Outline each blood parasite and name the species.
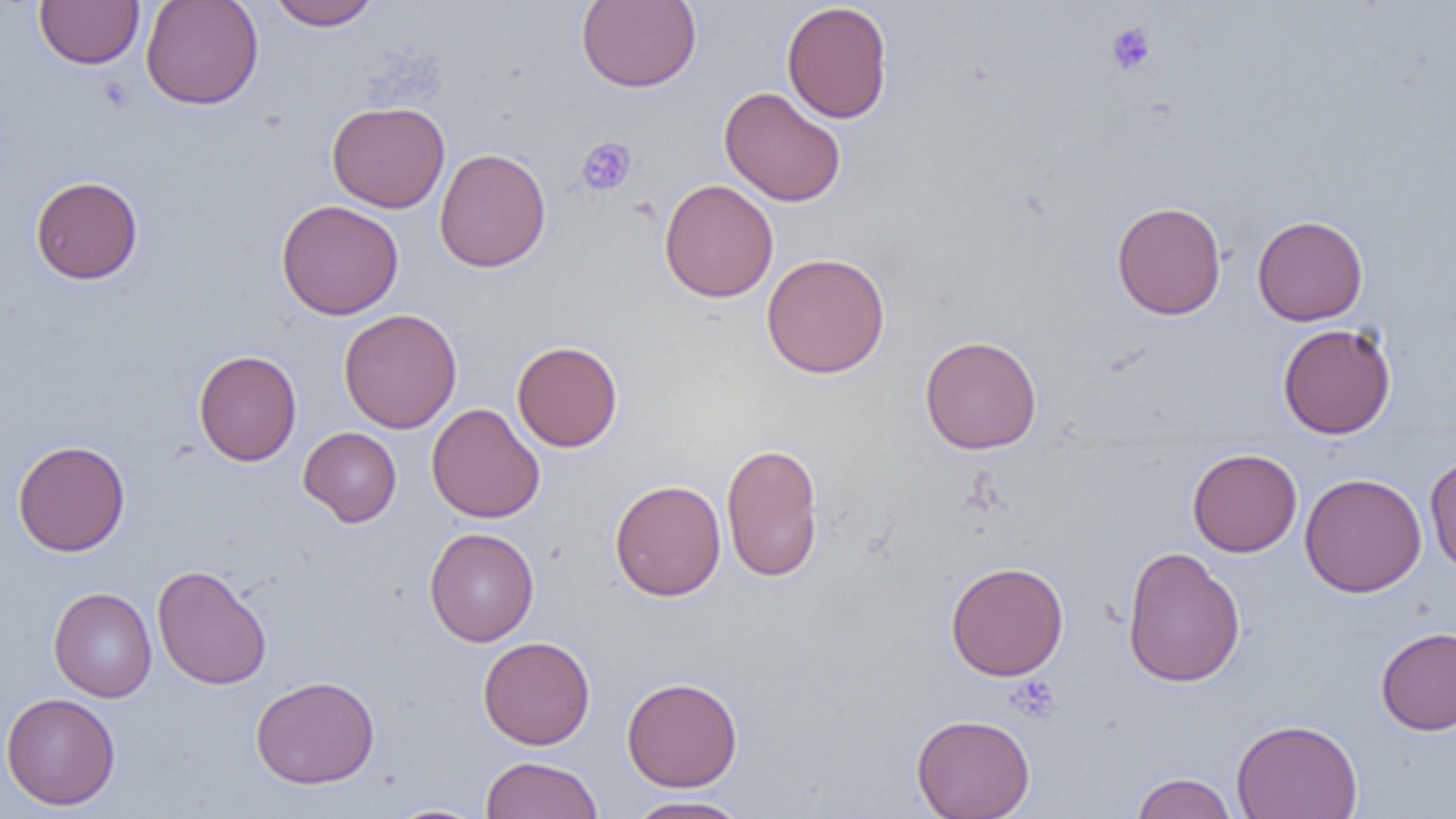
No blood parasites observed.

Summary:
  - Coordinate format: approximate bounding boxes as [x1, y1, x2, y2] in pixels
  - Uninfected red blood cell locations: [34, 0, 144, 69], [140, 0, 264, 110], [267, 0, 381, 30], [576, 0, 701, 92], [781, 1, 894, 124], [719, 86, 846, 207], [326, 101, 450, 213], [434, 147, 551, 272], [30, 176, 143, 285], [659, 179, 778, 302], [276, 200, 403, 320], [1111, 201, 1226, 320], [1252, 215, 1368, 326], [761, 253, 891, 379], [338, 309, 462, 433], [1277, 323, 1396, 439], [919, 335, 1041, 454], [511, 340, 623, 452], [193, 350, 302, 466], [426, 403, 545, 524], [298, 426, 402, 527], [12, 440, 130, 556], [721, 442, 824, 582], [1187, 448, 1302, 557], [1424, 452, 1456, 575], [1299, 472, 1427, 598], [609, 479, 726, 601], [424, 527, 539, 646], [1122, 545, 1245, 688], [945, 561, 1069, 680], [152, 564, 271, 690], [48, 588, 157, 702], [1375, 627, 1456, 735], [478, 636, 595, 750], [250, 675, 380, 789], [621, 676, 743, 792], [1, 692, 121, 810], [911, 713, 1035, 818], [1231, 718, 1363, 819], [481, 756, 603, 819], [1130, 772, 1238, 818], [624, 795, 752, 818], [380, 803, 493, 819]
  - Platelet locations: [1105, 21, 1157, 76], [576, 136, 638, 196], [1006, 676, 1061, 724]
  - Slide-level diagnosis: no evidence of blood parasites
  - Preparation: thin blood film
  - Image size: 1456×819 pixels
  - Magnification: 1000x
  - Field of view: single
  - Modality: optical microscopy